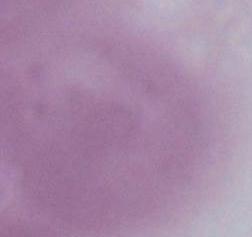
magnification = 1000x
modality = photomicrograph
identification = erythrocyte